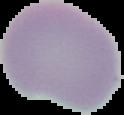

Summary:
  - Image size: 124×115 pixels
  - Malaria status: uninfected
  - Image type: cell region segmented out of the field of view; surrounding area masked to black
  - Preparation: thin blood smear